State the blood parasite species.
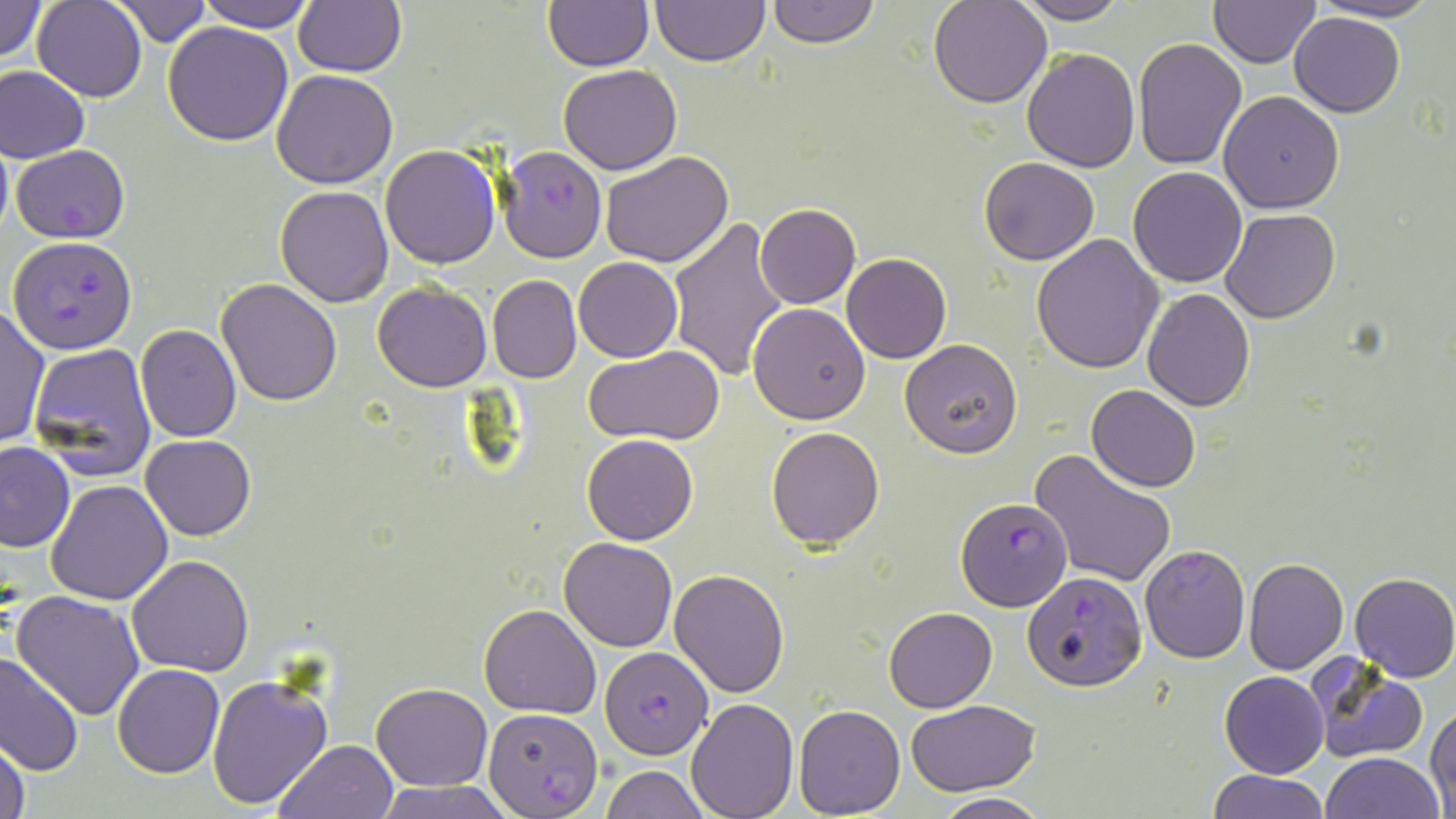

Plasmodium falciparum.

Summary:
  - Coordinate format: approximate bounding boxes as (x1,y1)-(x2,y2) corner pairs in pixels
  - Plasmodium falciparum-infected red blood cell locations: (11,145)-(131,244), (498,146)-(607,262), (8,236)-(137,355), (955,495)-(1072,608), (1022,573)-(1148,692), (600,647)-(713,760), (483,707)-(603,816)
  - Uninfected red blood cell locations: (0,0)-(48,62), (112,0)-(210,46), (197,0)-(316,32), (650,0)-(768,66), (765,0)-(879,49), (929,0)-(1052,107), (1013,0)-(1130,24), (1306,0)-(1445,24), (32,1)-(147,101), (293,1)-(407,76), (1208,1)-(1322,67), (543,2)-(653,70), (1288,11)-(1404,118), (163,22)-(294,146), (1132,39)-(1248,170), (1022,47)-(1140,172), (558,64)-(681,175), (1,66)-(90,163), (272,70)-(399,188), (1218,91)-(1345,212), (0,132)-(13,246), (379,143)-(501,268), (599,150)-(733,267), (979,156)-(1099,266), (1128,166)-(1247,287), (276,186)-(393,307), (755,203)-(860,309), (1222,210)-(1340,324), (666,212)-(789,382), (1032,233)-(1165,375), (842,253)-(952,363), (573,256)-(682,362), (487,275)-(582,385), (216,279)-(342,407), (372,281)-(492,392), (1141,288)-(1254,411), (748,303)-(871,425), (0,307)-(51,450), (140,307)-(324,432), (135,324)-(241,441), (899,340)-(1022,457), (28,343)-(157,480), (583,346)-(727,446), (1087,384)-(1200,492), (767,427)-(884,549), (141,433)-(256,540), (582,434)-(699,545), (0,442)-(75,552), (1028,448)-(1177,589), (46,480)-(173,604), (559,537)-(678,652), (1140,544)-(1251,664), (127,555)-(255,676), (1243,558)-(1349,674), (669,568)-(789,698), (1349,572)-(1456,683), (10,591)-(146,721), (479,602)-(601,717), (883,606)-(997,713), (0,651)-(83,777), (1309,657)-(1430,765), (112,664)-(225,779), (1219,671)-(1329,778), (206,675)-(332,811), (371,682)-(492,790), (684,698)-(799,818), (905,699)-(1041,795), (793,704)-(905,816), (1427,704)-(1456,811), (0,738)-(30,819), (274,738)-(399,819), (1321,752)-(1444,818), (602,765)-(707,819), (1206,769)-(1329,819), (374,780)-(515,819), (933,792)-(1048,818)
  - Modality: light microscopy
  - Preparation: thin blood smear
  - Stain: May-Grünwald-Giemsa
  - Magnification: 1000x
  - Field of view: single
  - Image size: 1456×819 pixels